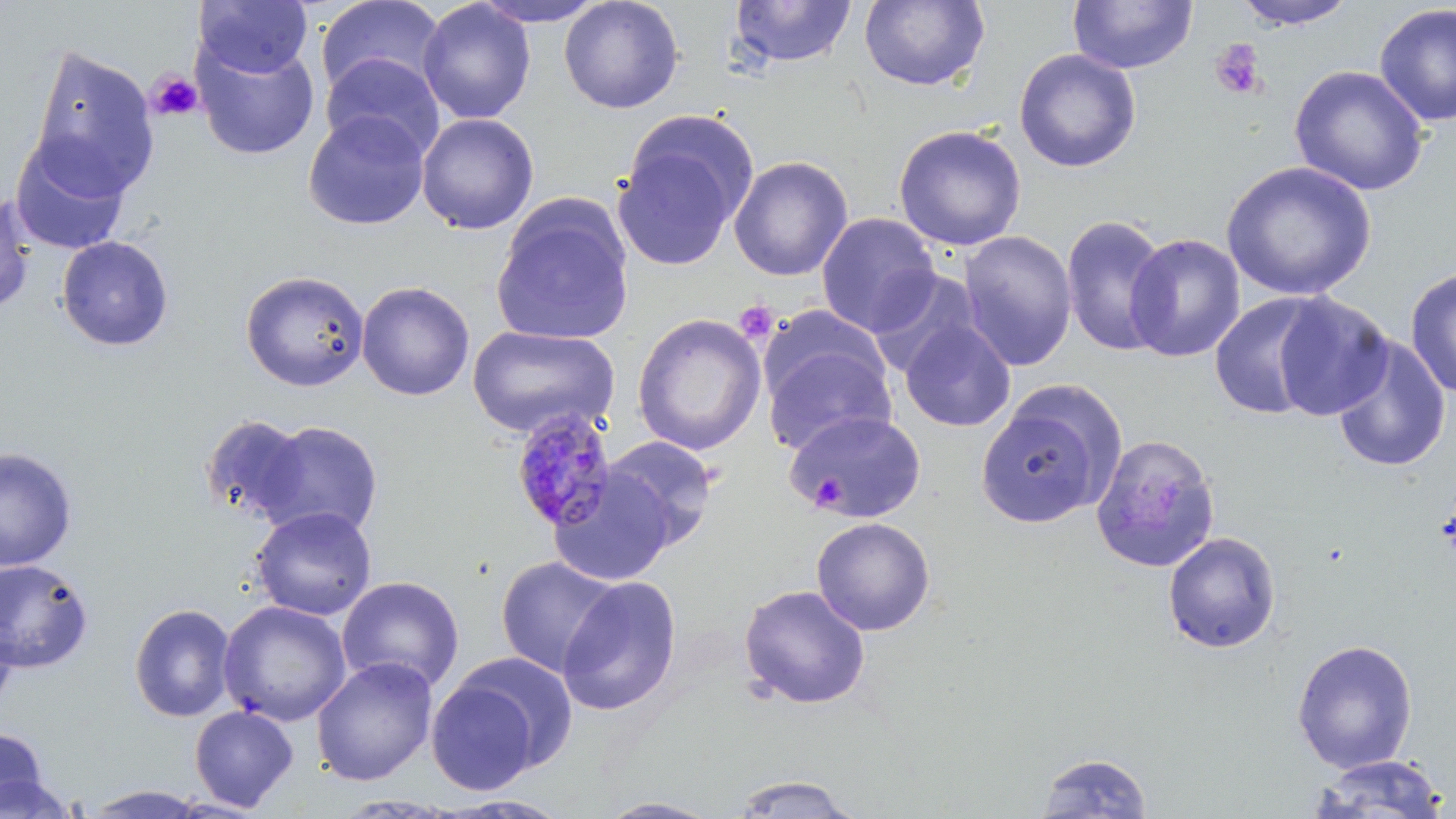

slide-level diagnosis = Plasmodium malariae
modality = light microscopy
field of view = one of a larger specimen
stain = May-Grünwald-Giemsa
preparation = thin blood film
image size = 1456×819 pixels
magnification = 1000x
Plasmodium malariae-infected red blood cell locations = approximate bounding boxes as [x1, y1, x2, y2] in pixels: [510, 407, 620, 534]
uninfected red blood cell locations = approximate bounding boxes as [x1, y1, x2, y2] in pixels: [194, 0, 313, 79], [315, 0, 444, 98], [471, 0, 609, 27], [559, 0, 685, 114], [858, 0, 990, 91], [1067, 0, 1198, 75], [1230, 0, 1359, 30], [417, 1, 536, 124], [728, 1, 858, 69], [1374, 3, 1455, 128], [192, 37, 320, 161], [27, 45, 160, 198], [1013, 48, 1141, 173], [320, 53, 445, 161], [1290, 65, 1430, 196], [302, 110, 431, 230], [416, 113, 539, 235], [614, 115, 756, 270], [893, 124, 1027, 251], [8, 134, 131, 256], [728, 155, 853, 282], [1220, 160, 1376, 301], [0, 192, 36, 313], [491, 197, 635, 347], [816, 213, 940, 336], [1060, 214, 1171, 358], [957, 231, 1077, 372], [1124, 233, 1245, 363], [56, 236, 174, 351], [1404, 267, 1456, 398], [867, 269, 984, 380], [240, 270, 370, 392], [356, 280, 475, 401], [1270, 292, 1394, 421], [1209, 293, 1334, 419], [631, 313, 767, 456], [899, 318, 1016, 432], [758, 321, 897, 458], [466, 325, 619, 440], [1330, 336, 1452, 474], [975, 388, 1123, 530], [783, 409, 927, 522], [198, 414, 310, 524], [253, 420, 385, 540], [1090, 433, 1221, 573], [601, 435, 720, 548], [0, 447, 78, 571], [547, 467, 678, 587], [251, 506, 377, 620], [811, 516, 935, 636], [1162, 531, 1282, 654], [495, 555, 621, 678], [0, 559, 94, 673], [337, 576, 465, 694], [556, 577, 682, 716], [738, 585, 871, 709], [217, 600, 352, 727], [129, 603, 236, 723], [0, 610, 18, 713], [1291, 639, 1418, 773], [452, 651, 579, 774], [311, 657, 438, 785], [425, 673, 544, 795], [189, 705, 299, 812], [0, 725, 50, 815], [1036, 751, 1153, 817], [1310, 754, 1452, 818], [0, 773, 79, 818], [729, 773, 861, 817], [83, 785, 211, 818], [439, 795, 572, 817], [597, 798, 723, 818]
platelet locations = approximate bounding boxes as [x1, y1, x2, y2] in pixels: [1210, 39, 1267, 100], [146, 69, 203, 122], [734, 300, 778, 343], [1436, 493, 1456, 565]